Assess for malaria.
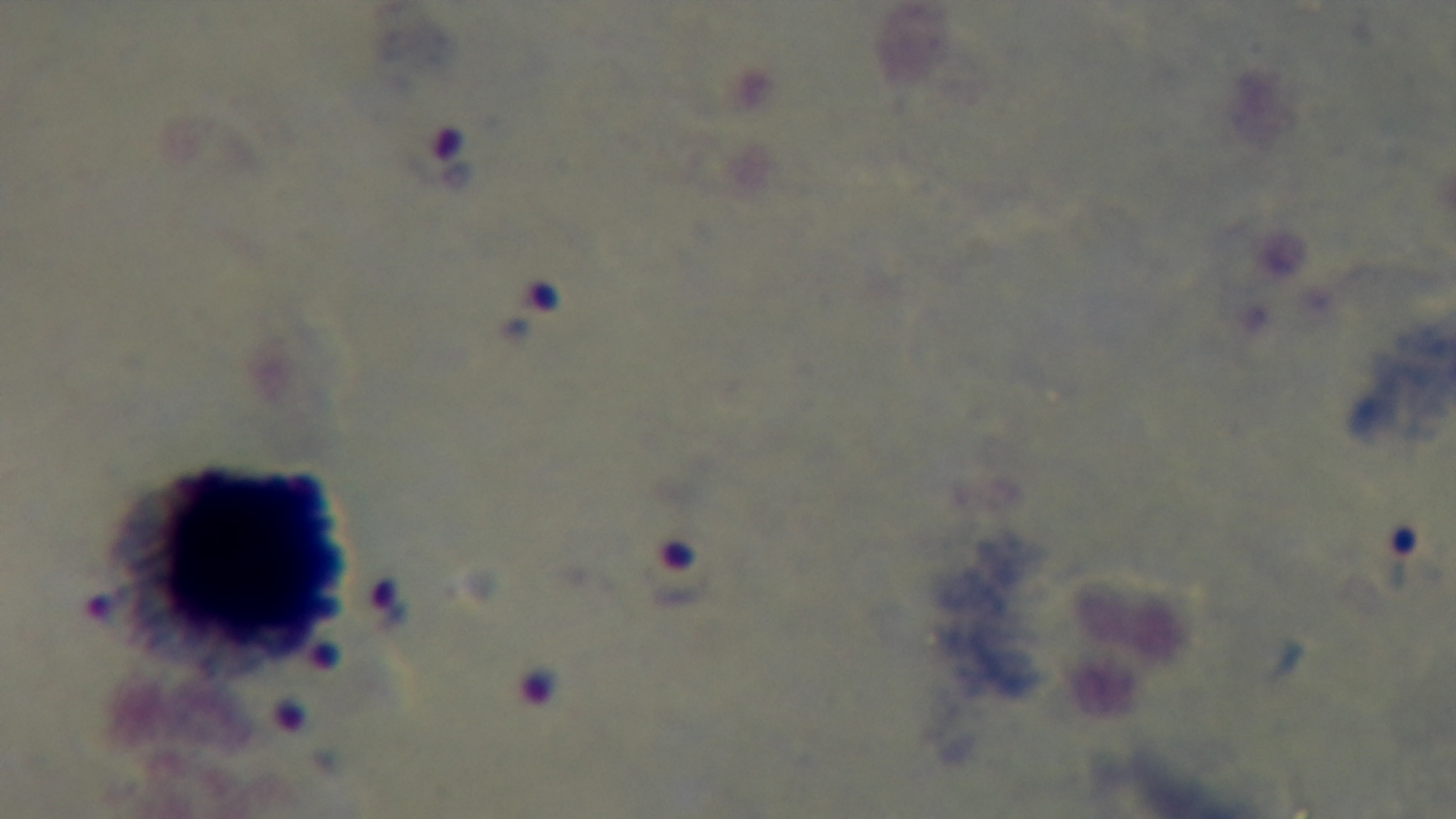

It is infected.

Light microscopy. Captured with a mounted 4K digital camera. 100x oil-immersion objective. Preparation: thick smear. Giemsa stain. One field from the slide.